Report the malaria status of this cell.
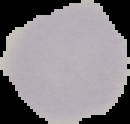

It is uninfected.

Summary:
  - Image type: cell region segmented out of the field of view; surrounding area masked to black
  - Preparation: thin blood film
  - Image size: 130×124 pixels